Identify the parasite.
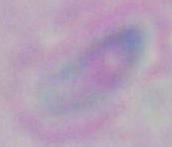

Toxoplasma gondii.

modality = micrograph
magnification = 1000x